Locate every leukocyte (white blood cell).
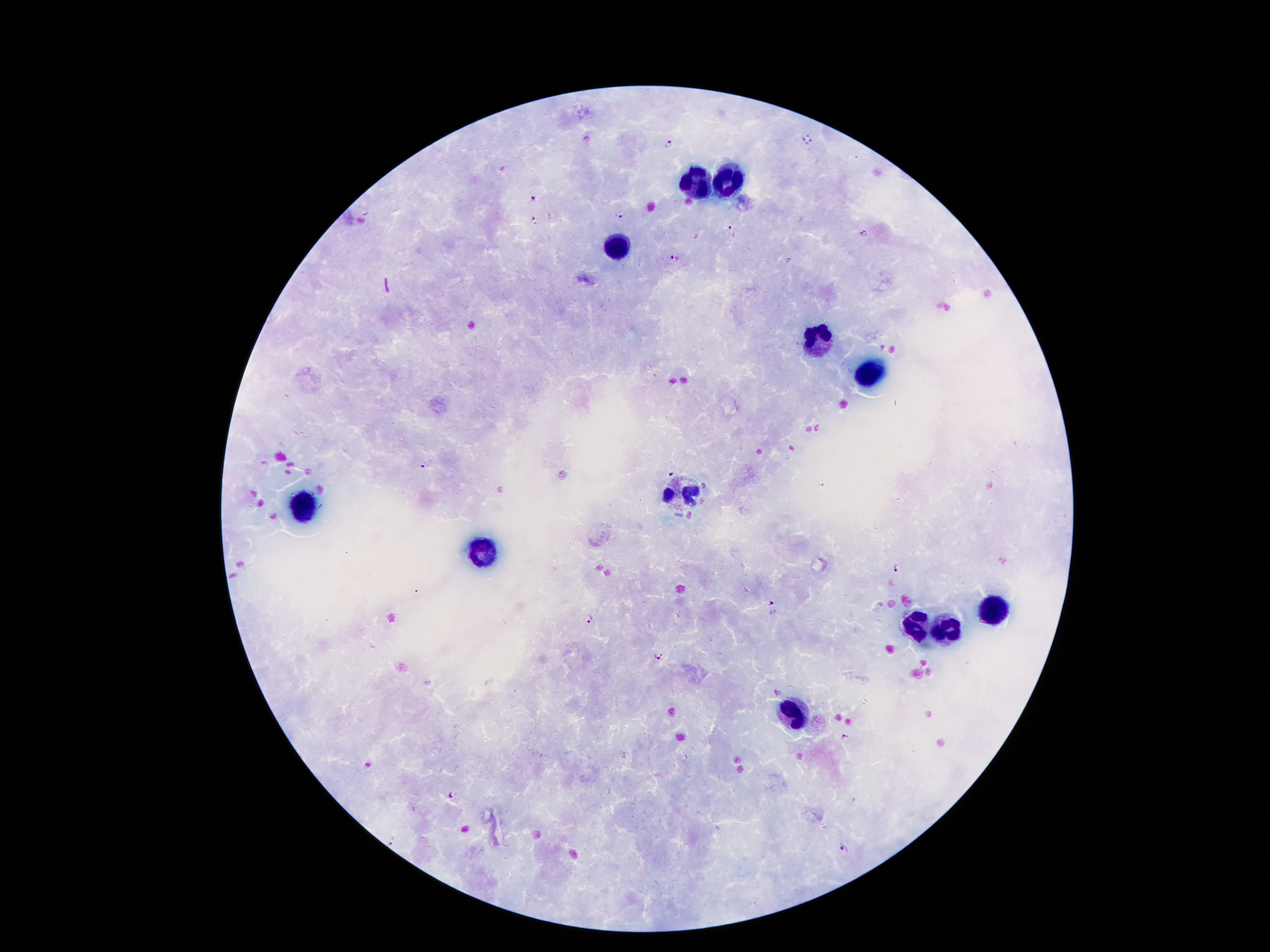

Approximate object centers, in pixels from the top-left corner.
Leukocytes: (x=732, y=180), (x=699, y=183), (x=615, y=248), (x=818, y=338), (x=870, y=372), (x=682, y=492), (x=303, y=505), (x=482, y=552), (x=990, y=609), (x=917, y=628), (x=950, y=628), (x=789, y=710).

Malaria parasite locations: (x=806, y=132), (x=799, y=139), (x=813, y=141), (x=669, y=145), (x=806, y=146), (x=535, y=198), (x=619, y=214), (x=533, y=221), (x=733, y=231), (x=865, y=234), (x=674, y=257), (x=428, y=465), (x=670, y=469), (x=899, y=570), (x=771, y=603), (x=588, y=619), (x=658, y=657), (x=846, y=738), (x=451, y=795), (x=396, y=843), (x=843, y=846). 100x magnification. Smartphone photograph taken through the microscope eyepiece. Single field of view. Patient malaria status: positive for Plasmodium falciparum. Image is 1270×952 pixels. Giemsa-stained preparation. Thick blood film.